Classify this cell by malaria status.
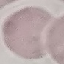
Uninfected.

Giemsa-stained preparation. Automatically extracted cell patch, resized to 64 × 64 pixels. Acquired by smartphone through the microscope eyepiece. Thin blood film.